State which parasite is depicted.
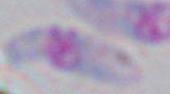
This is Toxoplasma gondii.

magnification: 1000x
modality: photomicrograph